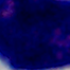
Summary:
  - Identification: leukocyte
  - Magnification: 1000x
  - Modality: photomicrograph